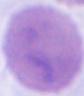
An erythrocyte is seen. Captured at 1000x magnification. Photomicrograph.